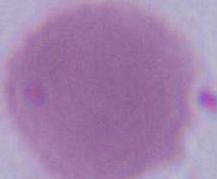

magnification = 1000x
identification = erythrocyte
modality = photomicrograph